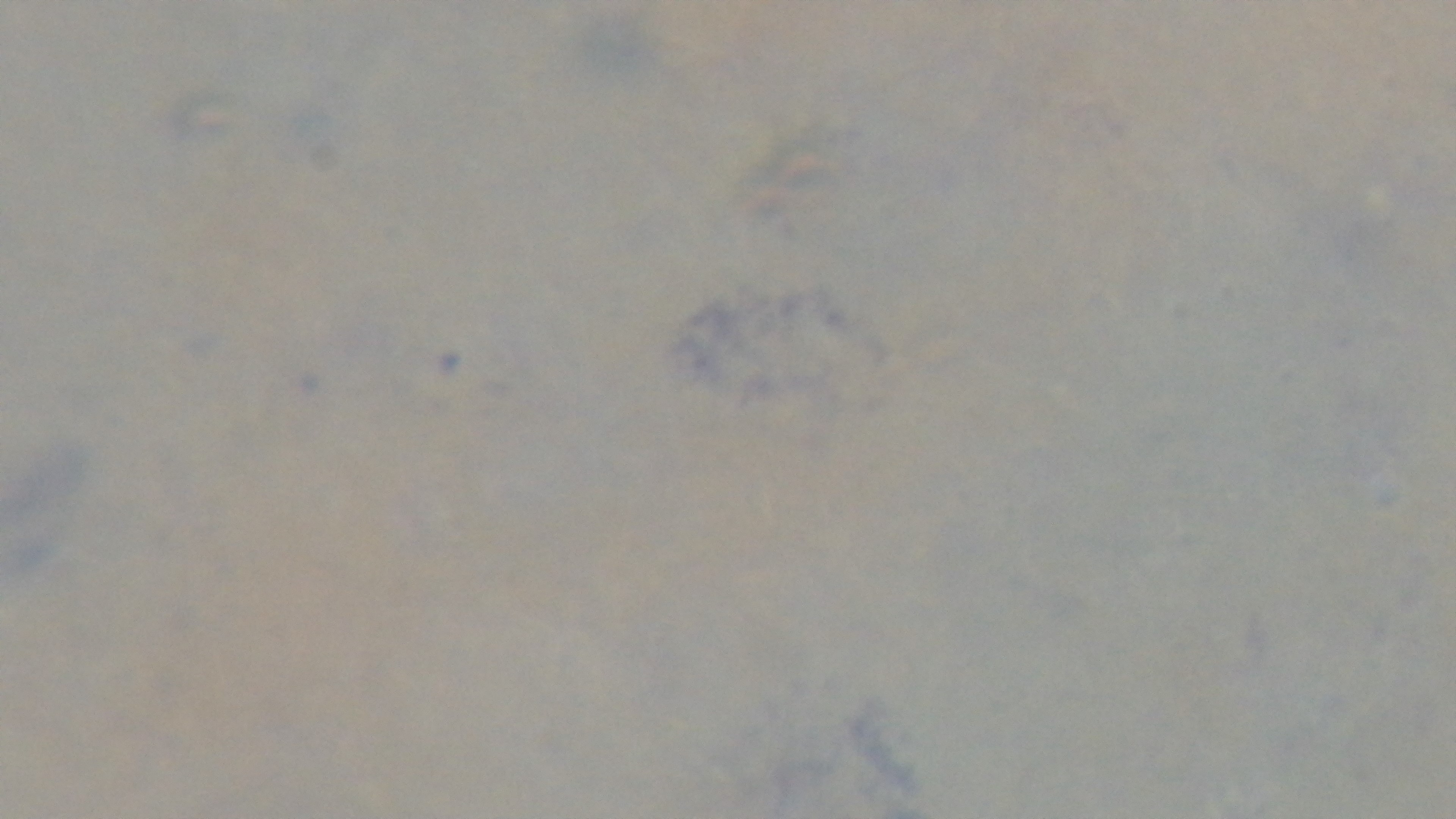
Summary:
  - Modality: light microscopy
  - Capture: mounted 4K digital camera
  - Field of view: single
  - Objective: 100x oil immersion
  - Preparation: thick blood film
  - Stain: Giemsa
  - Malaria status: uninfected